Report the malaria status of this cell.
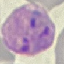
Parasitized.

Summary:
  - Stain: Giemsa
  - Image type: cell patch, automatically extracted from a larger field of view and resized to 64 × 64 pixels
  - Capture: smartphone camera at the microscope eyepiece
  - Preparation: thin blood smear